Locate every Plasmodium parasite.
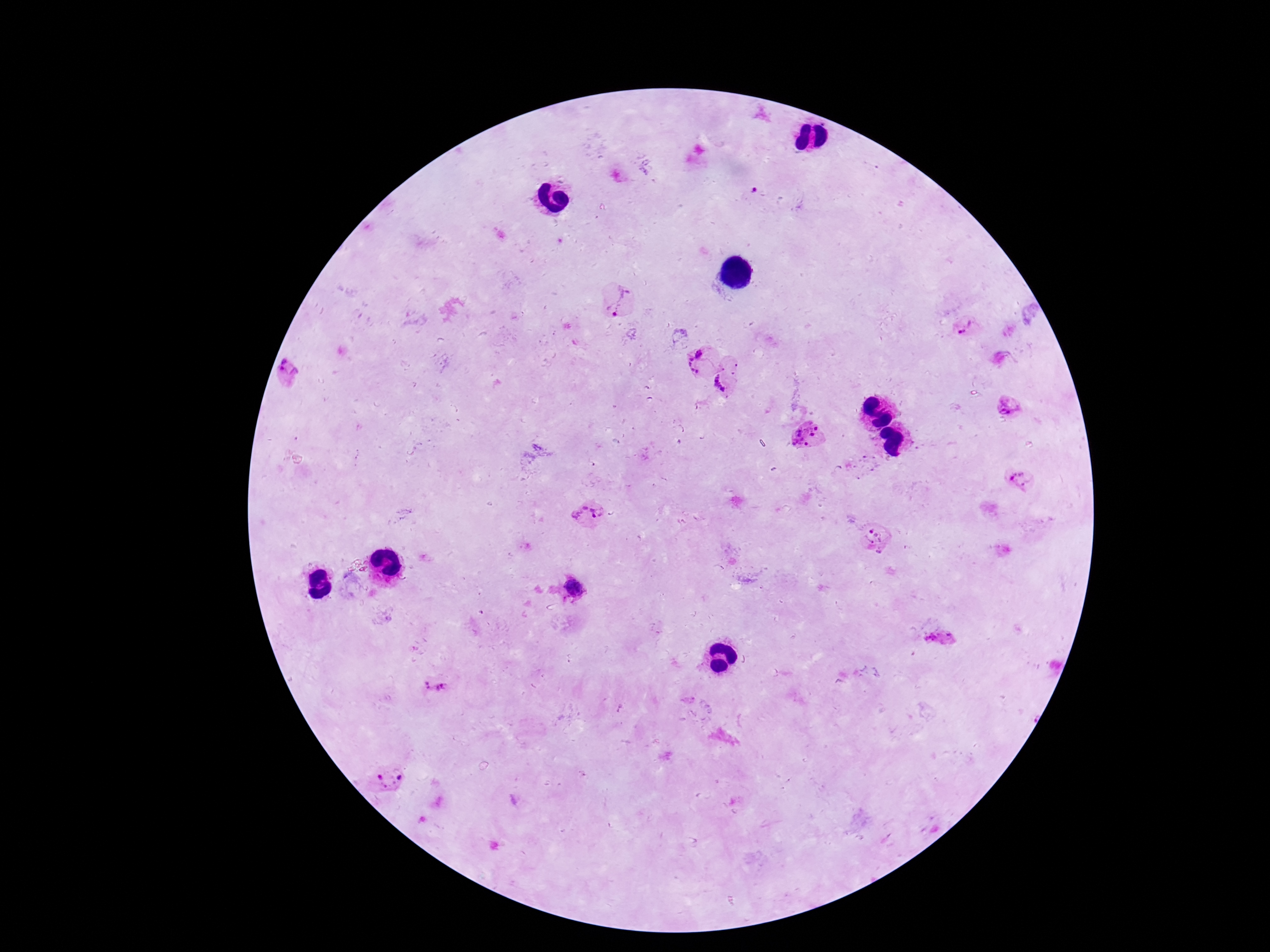
Approximate centers as {x, y} in pixels.
Plasmodium parasites: {621, 299}, {964, 326}, {700, 353}, {693, 366}, {291, 377}, {725, 381}, {1006, 405}, {804, 434}, {1019, 481}, {587, 513}, {878, 539}, {576, 588}, {940, 638}, {434, 686}, {391, 779}.

field of view = one from this slide
capture = smartphone camera through the microscope eyepiece
image size = 1270×952 pixels
magnification = 100x
preparation = thick blood film
stain = Giemsa
patient malaria status = positive